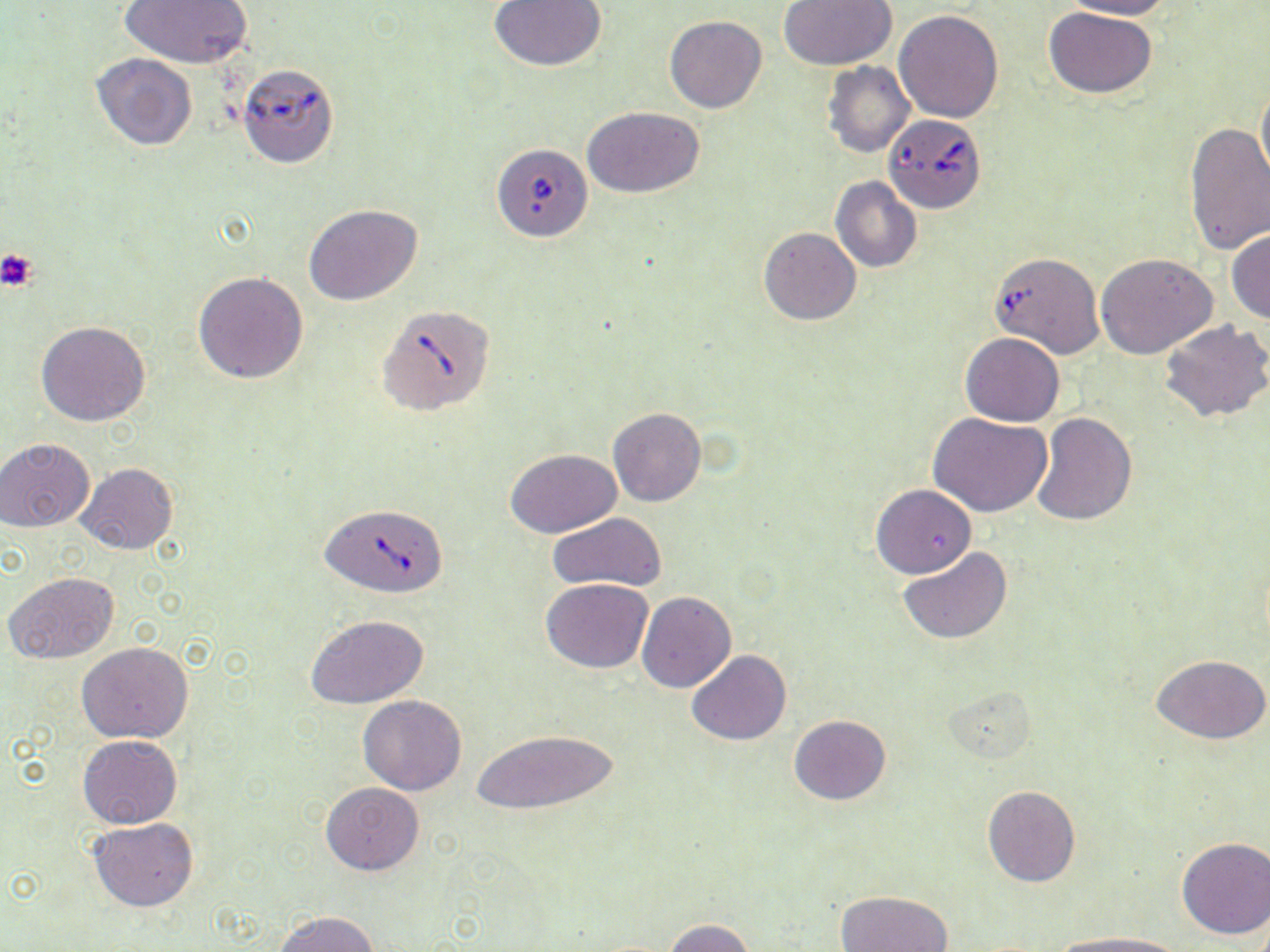
{
  "slide_level_diagnosis": "Babesia divergens",
  "modality": "optical microscopy",
  "image_size": "1270×952 pixels",
  "uninfected_red_blood_cell_locations": "approximate bounding boxes as (x1,y1)-(x2,y2) corner pairs in pixels: (119,0)-(253,69), (488,0)-(607,72), (779,0)-(897,70), (1060,0)-(1175,20), (1044,8)-(1157,98), (893,9)-(1004,123), (663,15)-(766,112), (90,53)-(199,151), (823,61)-(915,158), (1256,80)-(1270,190), (583,106)-(704,198), (1183,121)-(1270,254), (830,176)-(921,273), (304,204)-(423,305), (758,227)-(861,325), (1227,229)-(1270,324), (1096,254)-(1217,360), (192,271)-(308,383), (1159,318)-(1270,426), (35,322)-(150,427), (960,332)-(1064,425), (607,407)-(707,506), (929,413)-(1053,518), (1031,413)-(1137,526), (1,437)-(95,532), (505,449)-(621,538), (77,462)-(178,556), (872,484)-(976,579), (547,512)-(667,594), (897,547)-(1013,645), (3,571)-(120,664), (541,578)-(653,673), (637,591)-(737,692), (307,615)-(429,708), (77,642)-(194,743), (686,650)-(792,745), (1152,653)-(1269,744), (945,688)-(1038,765), (358,694)-(466,795), (789,715)-(891,805), (469,728)-(622,818), (78,735)-(182,829), (323,783)-(424,875), (982,786)-(1081,887), (87,817)-(199,912), (1176,837)-(1270,939), (837,890)-(955,952), (274,911)-(381,952), (661,918)-(757,952), (1050,932)-(1188,952)",
  "magnification": "1000x",
  "babesia_divergens_infected_red_blood_cell_locations": "approximate bounding boxes as (x1,y1)-(x2,y2) corner pairs in pixels: (241,70)-(335,168), (885,114)-(988,214), (491,143)-(593,243), (988,251)-(1104,359), (376,303)-(496,417), (321,502)-(448,597)",
  "stain": "May-Grünwald-Giemsa",
  "preparation": "thin blood smear",
  "field_of_view": "single",
  "platelet_locations": "approximate bounding boxes as (x1,y1)-(x2,y2) corner pairs in pixels: (0,248)-(40,292)"
}